State which parasite is depicted.
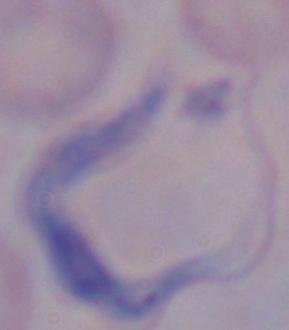
This is a trypanosome.

Summary:
  - Modality: photomicrograph
  - Magnification: 1000x